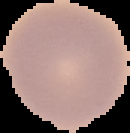

Malaria status: uninfected. Segmented cell region on a black background. From a thin blood smear. Image is 130×133 pixels.